Report the malaria status of this cell.
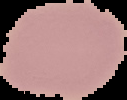
Uninfected.

Summary:
  - Image type: segmented cell region with the area outside set to black
  - Image size: 127×100 pixels
  - Preparation: thin blood smear